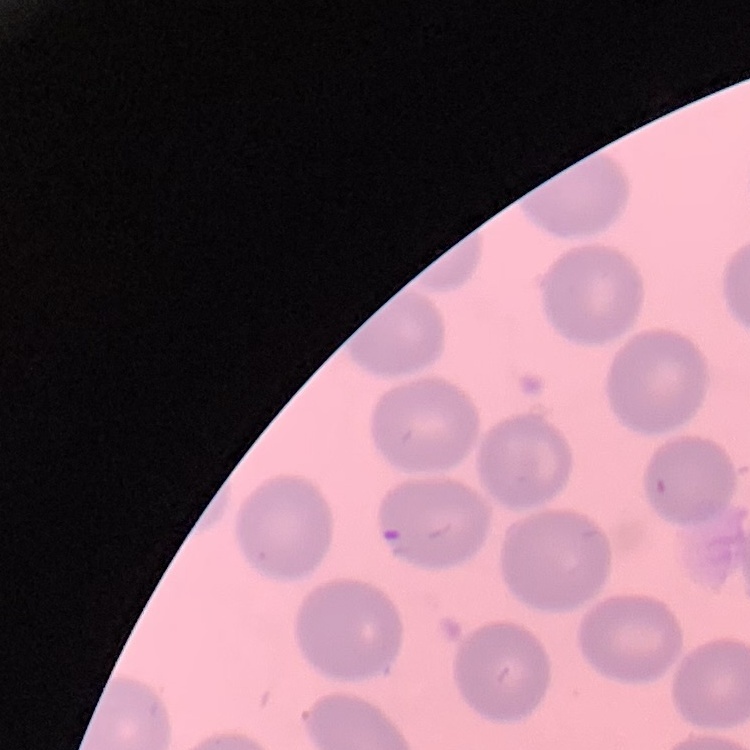

The red blood cells show no rouleaux formation. Thin blood smear. Stained with either Field's or Giemsa. One tile cut from a larger photomicrograph.